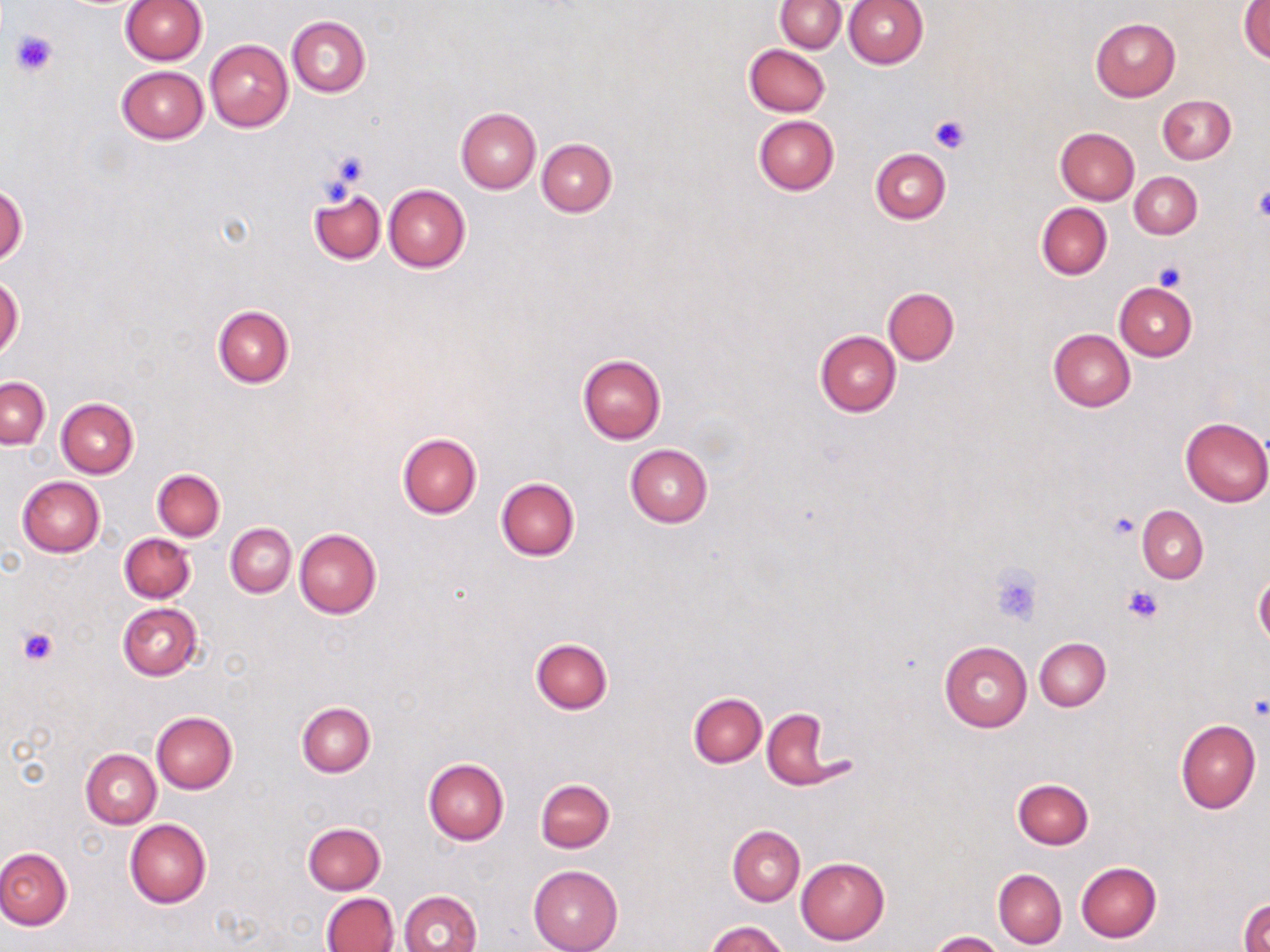
slide-level diagnosis = negative for blood parasites
image size = 1270×952 pixels
preparation = thin blood film
magnification = 1000x
modality = light microscopy
platelet locations = approximate bounding boxes as (x1,y1)-(x2,y2) corner pairs in pixels: (9,30)-(56,79), (929,114)-(971,155), (325,148)-(371,191), (1253,186)-(1270,223), (1153,260)-(1186,290), (1109,513)-(1137,540), (990,563)-(1043,625), (1123,584)-(1165,624), (18,627)-(57,665)
field of view = one of a larger specimen
stain = May-Grünwald-Giemsa
uninfected red blood cell locations = approximate bounding boxes as (x1,y1)-(x2,y2) corner pairs in pixels: (843,0)-(927,70), (120,1)-(206,65), (776,1)-(845,53), (1239,2)-(1270,63), (287,17)-(370,97), (1091,18)-(1180,100), (205,39)-(292,132), (743,44)-(830,116), (117,67)-(208,144), (1158,95)-(1235,165), (455,107)-(541,193), (755,116)-(839,195), (1055,127)-(1139,205), (537,139)-(616,216), (870,148)-(950,223), (1129,172)-(1202,238), (384,184)-(470,272), (0,185)-(27,266), (308,190)-(385,264), (1036,204)-(1111,279), (0,276)-(24,360), (1114,282)-(1196,360), (883,287)-(958,365), (213,305)-(293,387), (1048,329)-(1135,411), (815,331)-(901,417), (578,354)-(665,445), (0,377)-(50,448), (57,398)-(138,477), (1180,416)-(1270,506), (397,432)-(481,518), (625,445)-(712,528), (152,469)-(224,540), (16,476)-(104,556), (496,478)-(579,561), (1137,506)-(1208,583), (226,523)-(296,597), (295,528)-(381,620), (119,533)-(195,603), (1254,573)-(1269,649), (117,603)-(203,681), (1034,637)-(1111,711), (530,638)-(612,714), (939,642)-(1031,732), (688,693)-(766,767), (297,702)-(375,776), (762,709)-(849,790), (151,712)-(237,793), (1175,719)-(1260,813), (81,749)-(161,828), (422,757)-(509,845), (535,778)-(615,852), (1012,779)-(1093,849), (125,818)-(211,907), (303,822)-(386,893), (727,826)-(805,905), (0,845)-(72,930), (796,856)-(890,944), (1075,861)-(1161,942), (529,865)-(622,952), (993,869)-(1066,949), (399,891)-(482,952), (322,892)-(399,952), (1240,898)-(1270,952), (707,920)-(787,952), (928,930)-(1004,951)